Assess the morphology of the red blood cells.
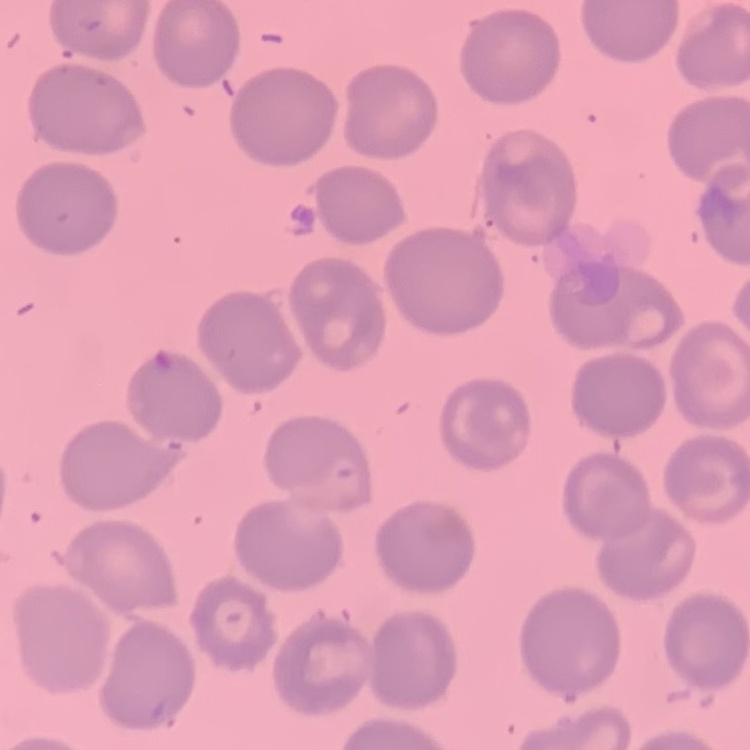
No rouleaux formation.

image type = square crop of a larger photomicrograph
stain = Field's or Giemsa
preparation = thin peripheral smear